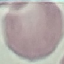
result = no malaria parasites seen
image type = cell patch, automatically extracted from a larger field of view and resized to 64 × 64 pixels
capture = smartphone camera at the microscope eyepiece
preparation = thin blood smear
stain = Giemsa